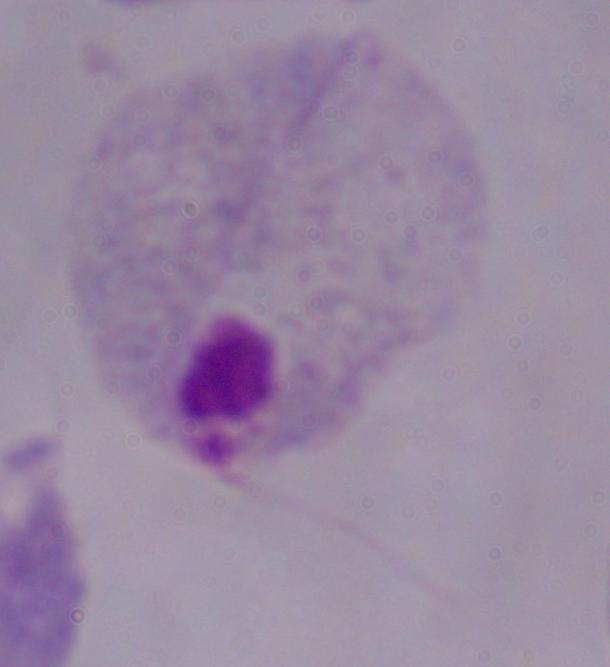

modality = photomicrograph
identification = trichomonad
magnification = 1000x